Identify the parasite.
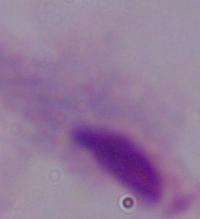

A trichomonad.

Micrograph. Captured at 1000x magnification.